Assess this cell for malaria.
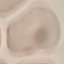

It is uninfected.

Acquired by smartphone through the microscope eyepiece. Thin blood smear. Automatically extracted cell patch, resized to 64 × 64 pixels. Giemsa stain.